Identify the parasite.
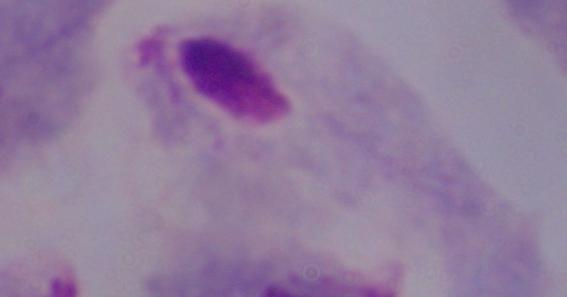
This is a trichomonad.

magnification = 1000x
modality = micrograph